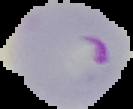

preparation = thin blood film
result = malaria parasites detected
image size = 133×109 pixels
image type = segmented cell region with the area outside set to black